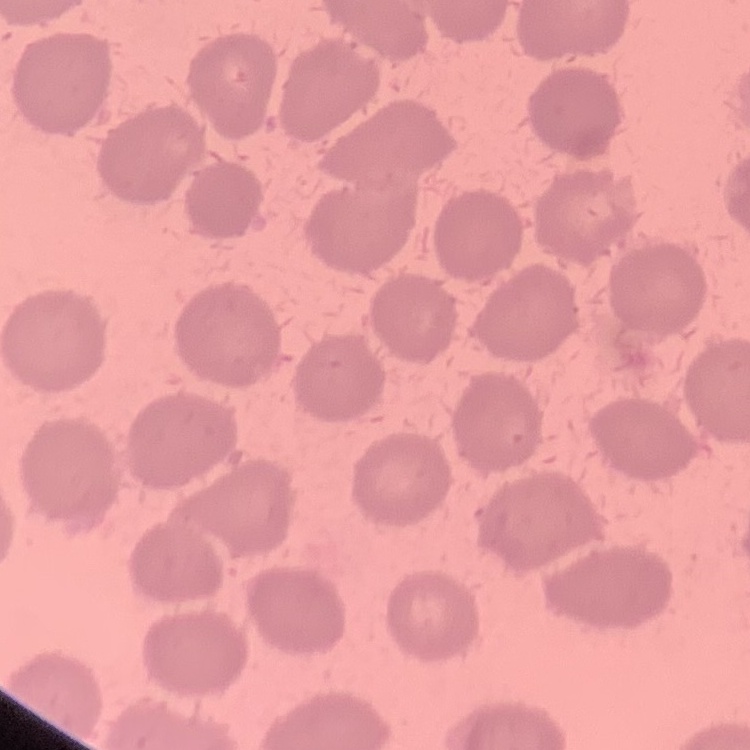

red blood cell morphology = no rouleaux formation
stain = Field's or Giemsa
preparation = thin blood smear
image type = square crop of a larger photomicrograph